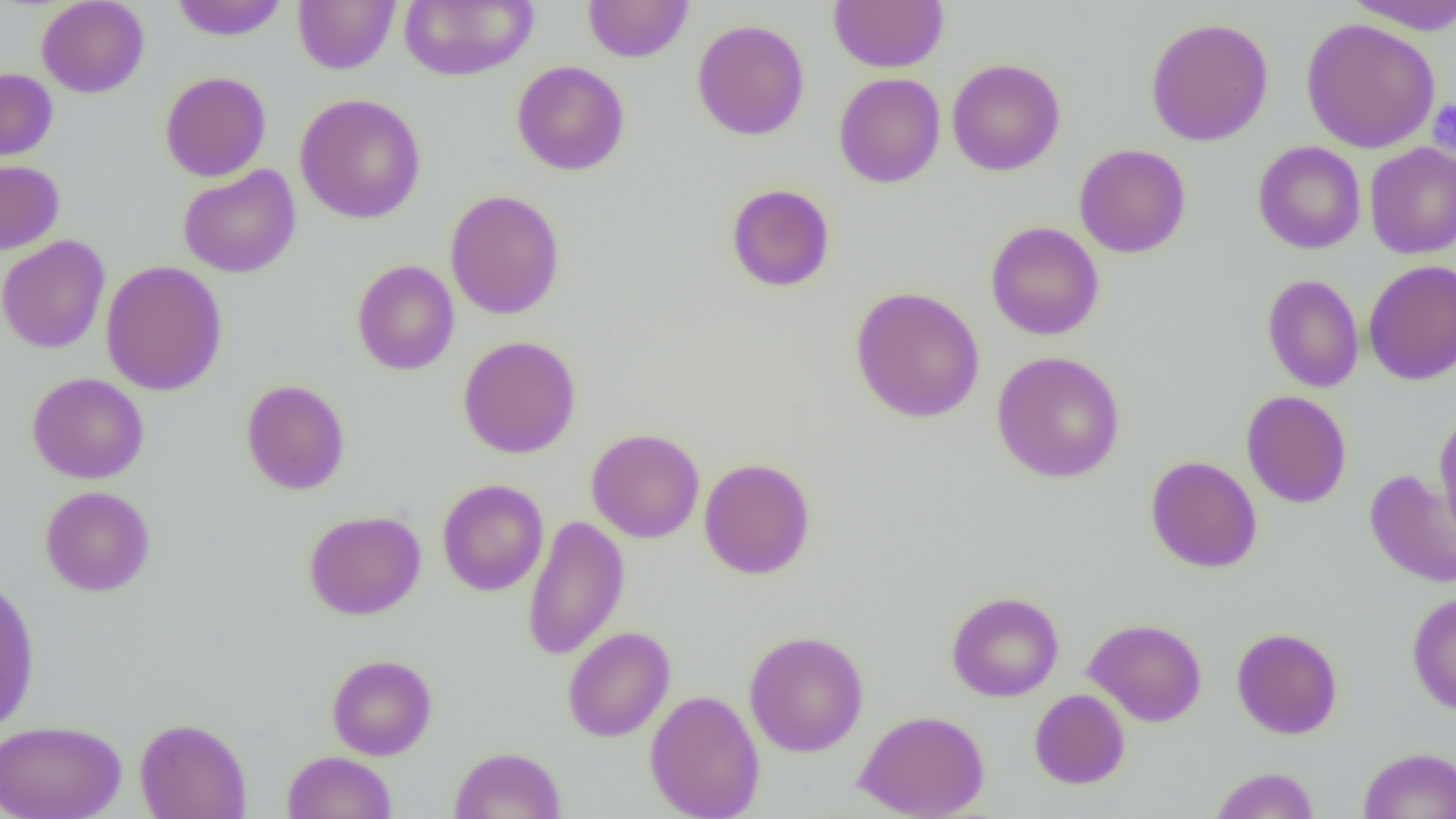
Summary:
  - Coordinate format: approximate bounding boxes as (x1, y1, x2, y2) in pixels
  - Platelet locations: (1427, 99, 1456, 155)
  - Uninfected red blood cell locations: (170, 0, 288, 41), (293, 0, 400, 74), (399, 0, 539, 82), (583, 0, 693, 62), (829, 0, 949, 73), (1344, 0, 1456, 35), (36, 1, 149, 98), (1145, 17, 1274, 147), (1300, 17, 1440, 154), (692, 19, 810, 141), (947, 58, 1065, 177), (511, 61, 629, 176), (0, 68, 58, 161), (159, 71, 271, 182), (833, 72, 945, 188), (295, 94, 427, 224), (1253, 141, 1366, 254), (1365, 142, 1456, 259), (1074, 143, 1191, 258), (0, 159, 64, 254), (178, 164, 301, 278), (725, 184, 836, 292), (445, 189, 565, 320), (986, 221, 1104, 341), (0, 235, 110, 353), (1363, 259, 1456, 386), (101, 260, 228, 396), (351, 260, 459, 375), (1262, 274, 1364, 393), (850, 286, 985, 424), (458, 335, 582, 459), (991, 351, 1126, 483), (27, 372, 149, 484), (241, 379, 351, 495), (1241, 390, 1352, 509), (1434, 413, 1456, 541), (586, 428, 705, 543), (1146, 455, 1262, 573), (698, 457, 816, 579), (1364, 469, 1456, 589), (437, 478, 548, 596), (40, 485, 155, 596), (303, 510, 426, 620), (522, 513, 629, 661), (0, 577, 40, 734), (1406, 590, 1456, 716), (946, 591, 1064, 702), (1084, 618, 1207, 727), (562, 625, 676, 742), (1231, 627, 1343, 739), (744, 630, 869, 757), (326, 654, 437, 760), (645, 689, 765, 819), (1029, 689, 1130, 789), (854, 709, 990, 819), (135, 716, 252, 819), (0, 719, 126, 819), (449, 747, 566, 818), (1358, 747, 1456, 819), (283, 750, 397, 819), (1209, 766, 1320, 819)
  - Slide-level diagnosis: negative for blood parasites
  - Image size: 1456×819 pixels
  - Preparation: thin blood smear
  - Magnification: 1000x
  - Modality: light microscopy
  - Field of view: one of a larger specimen